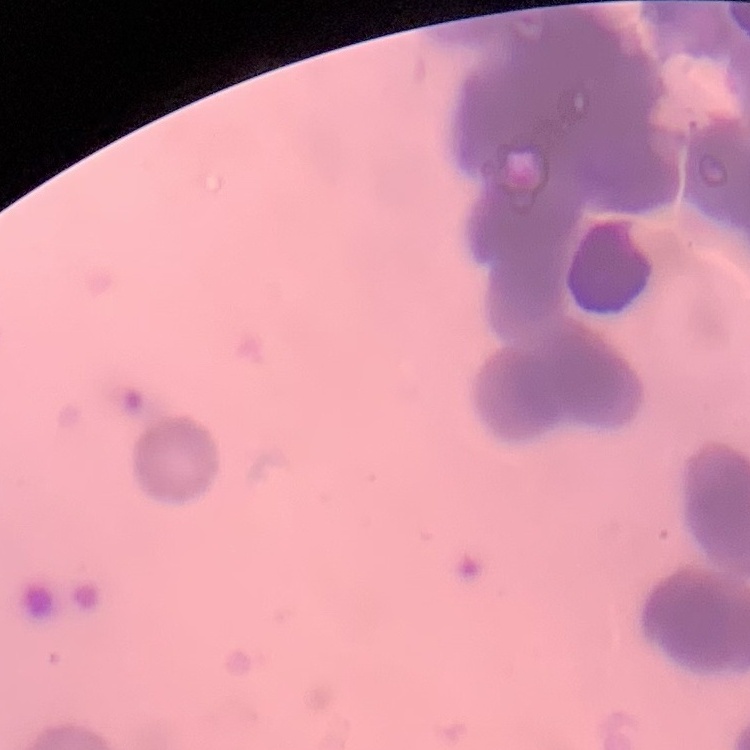

Summary:
  - Red blood cell morphology: rouleaux formation
  - Preparation: thin peripheral smear
  - Stain: Field's or Giemsa
  - Image type: one tile cut from a larger photomicrograph